Identify the blood parasite species.
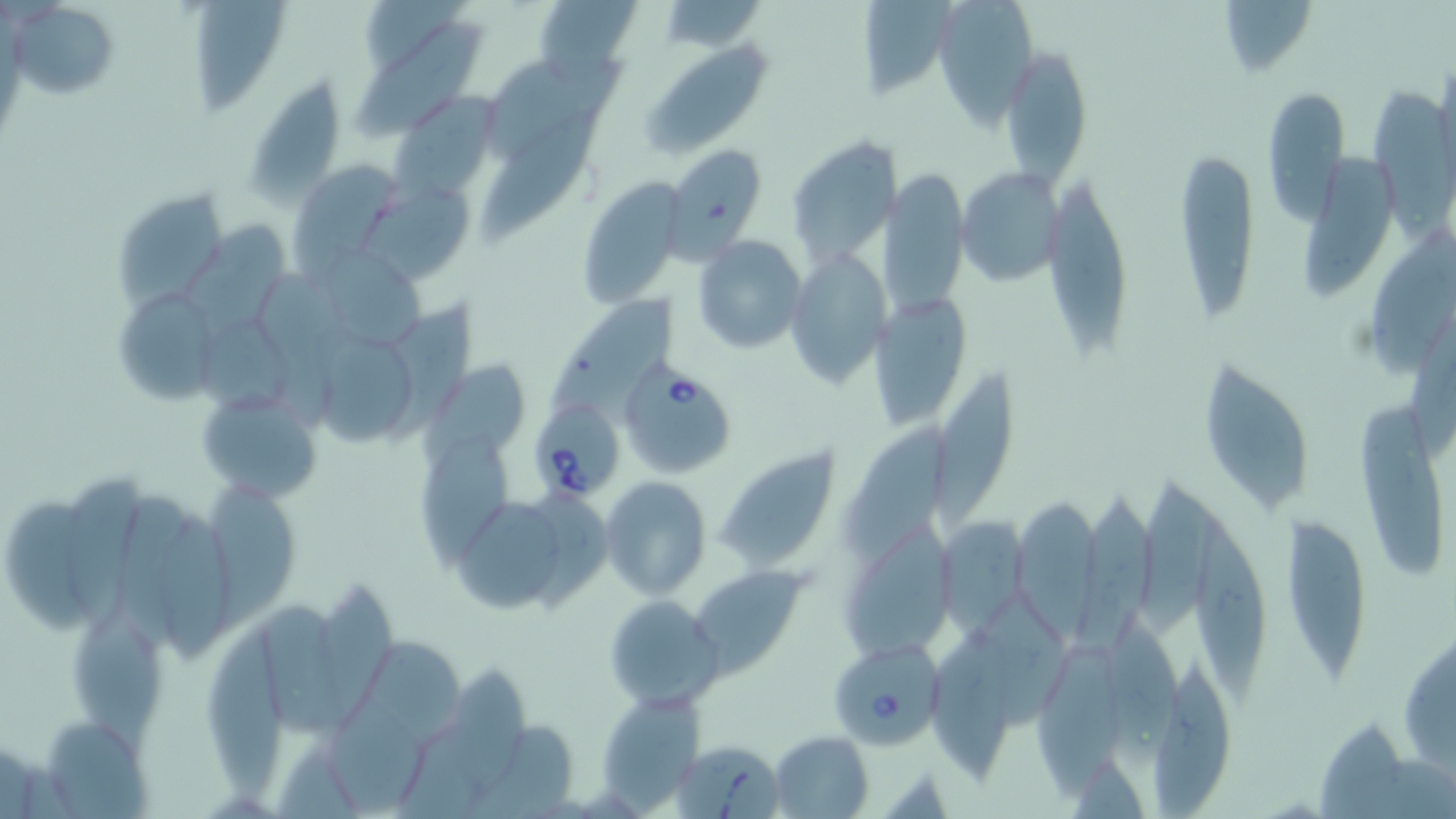

Babesia divergens.

image size = 1456×819 pixels
modality = light microscopy
Babesia divergens-infected red blood cell locations = approximate bounding boxes as (x1, y1, x2, y2) in pixels: (622, 362, 739, 480), (533, 398, 621, 498), (834, 641, 943, 750), (671, 737, 785, 817)
preparation = thin blood smear
stain = May-Grünwald-Giemsa
magnification = 1000x
field of view = single
uninfected red blood cell locations = approximate bounding boxes as (x1, y1, x2, y2) in pixels: (535, 0, 639, 85), (656, 0, 765, 49), (935, 0, 1039, 119), (1215, 0, 1316, 81), (185, 1, 293, 114), (13, 3, 119, 103), (861, 3, 948, 99), (349, 19, 485, 143), (640, 39, 775, 159), (1000, 42, 1093, 189), (479, 53, 626, 154), (244, 73, 347, 201), (1262, 86, 1349, 224), (1368, 86, 1452, 240), (391, 94, 498, 201), (481, 110, 602, 244), (786, 136, 897, 268), (1304, 139, 1398, 302), (664, 143, 767, 258), (1173, 148, 1259, 326), (289, 156, 402, 266), (877, 161, 964, 316), (955, 165, 1064, 286), (577, 176, 684, 308), (1042, 176, 1134, 367), (370, 180, 475, 284), (109, 187, 229, 313), (185, 215, 293, 329), (1367, 232, 1455, 383), (695, 236, 807, 353), (783, 247, 887, 388), (324, 253, 426, 347), (259, 268, 345, 393), (533, 287, 680, 418), (110, 288, 216, 404), (873, 291, 967, 431), (391, 298, 480, 448), (196, 316, 299, 420), (312, 331, 412, 446), (421, 359, 525, 470), (1203, 362, 1314, 511), (934, 365, 1019, 531), (198, 384, 324, 503), (1352, 399, 1446, 580), (839, 421, 944, 556), (416, 431, 511, 575), (716, 450, 841, 571), (1135, 465, 1216, 632), (63, 472, 139, 645), (600, 476, 712, 597), (205, 481, 293, 632), (115, 488, 185, 652), (528, 488, 615, 615), (1080, 489, 1149, 654), (458, 492, 562, 618), (1018, 496, 1096, 645), (8, 497, 103, 632), (155, 500, 225, 666), (1190, 504, 1266, 717), (935, 512, 1024, 639), (1282, 516, 1373, 685), (832, 531, 956, 660), (691, 563, 807, 672), (315, 577, 389, 725), (970, 582, 1072, 729), (603, 594, 725, 709), (258, 602, 336, 736), (1099, 608, 1186, 778), (65, 610, 169, 765), (203, 620, 282, 806), (933, 628, 1005, 785), (1402, 629, 1455, 779), (1033, 630, 1119, 796), (358, 632, 460, 749), (439, 659, 523, 796), (1148, 659, 1234, 813), (594, 694, 702, 809), (321, 701, 429, 814), (1312, 712, 1403, 817), (38, 713, 152, 815), (464, 720, 572, 819), (770, 730, 871, 817)